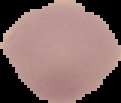

Summary:
  - Image type: cell region segmented out of the field of view; surrounding area masked to black
  - Image size: 121×103 pixels
  - Preparation: thin blood smear
  - Result: negative for Plasmodium parasites